Assess this cell for malaria.
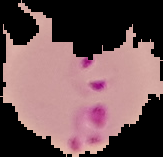

It is parasitized.

Summary:
  - Preparation: thin blood film
  - Image type: segmented cell region on a black background
  - Image size: 163×157 pixels